Locate platelets.
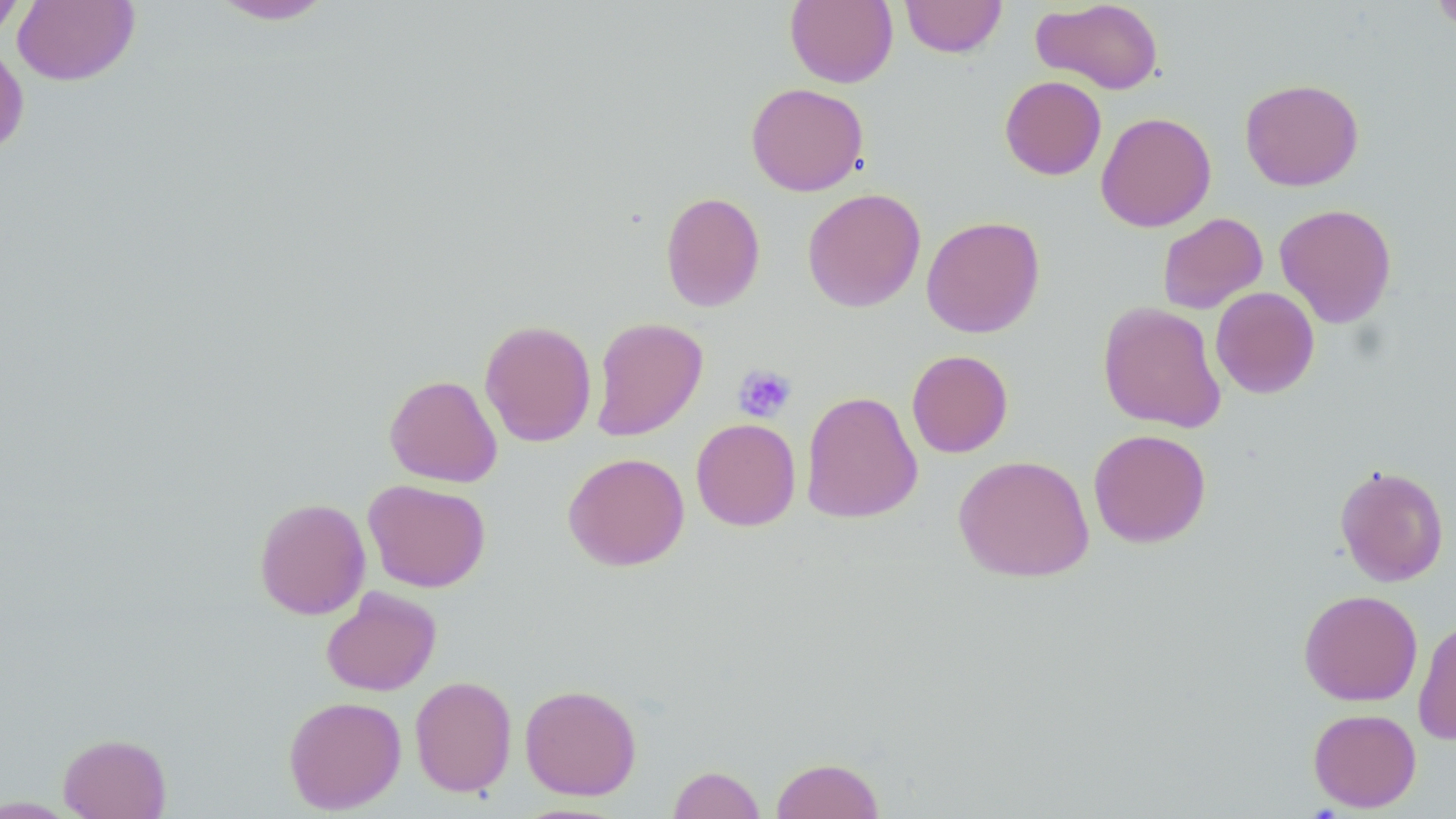

Approximate bounding boxes as (x1,y1)-(x2,y2) corner pairs in pixels.
Platelets: (733,364)-(797,422).

Summary:
  - Uninfected red blood cell locations: (12,0)-(140,86), (206,0)-(338,25), (785,0)-(898,88), (900,0)-(1007,58), (1032,0)-(1164,95), (1431,0)-(1456,35), (0,1)-(25,42), (0,41)-(29,159), (1000,75)-(1106,180), (1239,78)-(1364,191), (746,82)-(868,196), (1095,112)-(1217,232), (802,187)-(926,312), (660,191)-(765,312), (1274,203)-(1397,328), (1156,212)-(1268,314), (921,215)-(1045,338), (1210,287)-(1320,398), (1098,301)-(1226,433), (590,317)-(708,441), (479,319)-(597,447), (907,350)-(1013,458), (384,374)-(502,487), (800,390)-(923,524), (691,418)-(801,531), (1088,428)-(1212,548), (563,452)-(689,571), (953,454)-(1094,582), (1335,464)-(1449,587), (363,479)-(491,592), (254,497)-(371,620), (320,587)-(442,696), (1298,589)-(1423,706), (1413,618)-(1456,745), (409,675)-(517,797), (520,684)-(642,800), (283,695)-(406,813), (1308,708)-(1421,812), (58,732)-(172,818), (770,756)-(885,818), (667,765)-(765,819), (0,796)-(78,817)
  - Slide-level diagnosis: negative for blood parasites
  - Field of view: single
  - Preparation: thin blood smear
  - Image size: 1456×819 pixels
  - Stain: May-Grünwald-Giemsa
  - Magnification: 1000x
  - Modality: light microscopy